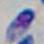 1000x magnification. Toxoplasma gondii is shown. Micrograph.